State the blood parasite species.
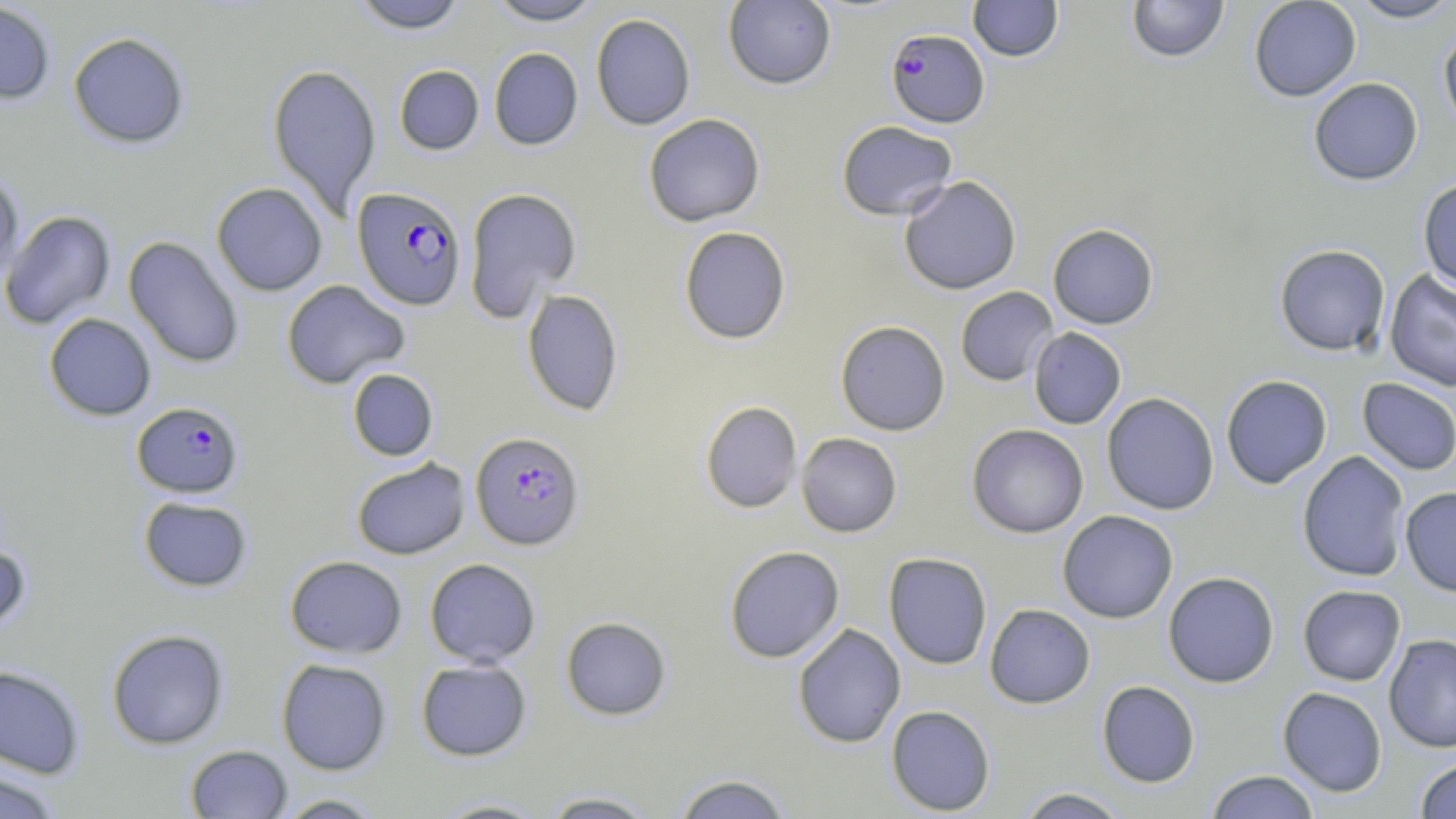
Plasmodium falciparum.

field of view = one of a larger specimen
magnification = 1000x
stain = May-Grünwald-Giemsa
uninfected red blood cell locations = approximate bounding boxes as [x1, y1, x2, y2] in pixels: [486, 0, 603, 25], [723, 0, 837, 90], [967, 0, 1064, 62], [1127, 0, 1229, 63], [1248, 0, 1362, 102], [1347, 0, 1456, 23], [0, 1, 57, 105], [350, 1, 468, 33], [590, 13, 696, 130], [1439, 27, 1456, 138], [68, 31, 190, 149], [489, 47, 583, 150], [267, 63, 382, 219], [394, 65, 484, 155], [1308, 77, 1423, 186], [643, 113, 765, 226], [836, 120, 958, 221], [0, 172, 25, 287], [898, 176, 1021, 295], [1418, 178, 1456, 293], [211, 182, 328, 296], [463, 187, 581, 322], [1, 210, 116, 330], [1047, 224, 1159, 329], [678, 226, 791, 344], [123, 235, 244, 369], [1274, 244, 1391, 357], [1385, 270, 1456, 391], [281, 279, 410, 389], [955, 286, 1058, 387], [522, 289, 624, 416], [43, 313, 156, 420], [835, 320, 950, 436], [1028, 327, 1126, 429], [347, 369, 438, 461], [1220, 374, 1332, 489], [1357, 378, 1456, 476], [1102, 392, 1219, 515], [700, 401, 803, 514], [966, 424, 1089, 538], [796, 433, 902, 537], [1297, 451, 1410, 582], [351, 457, 470, 560], [1400, 486, 1456, 597], [138, 496, 253, 592], [1057, 510, 1178, 623], [0, 541, 32, 638], [723, 545, 845, 663], [883, 552, 992, 669], [284, 555, 407, 658], [424, 558, 541, 667], [1163, 571, 1280, 688], [1298, 584, 1406, 686], [984, 603, 1095, 709], [560, 616, 671, 720], [792, 624, 906, 748], [106, 628, 229, 749], [1384, 633, 1456, 753], [276, 658, 392, 775], [415, 658, 532, 761], [0, 664, 86, 779], [1096, 680, 1200, 787], [1278, 687, 1387, 796], [886, 704, 996, 816], [185, 744, 292, 818], [1415, 757, 1456, 818], [0, 769, 62, 819], [1205, 770, 1320, 818], [671, 773, 794, 818], [1013, 787, 1131, 818], [539, 791, 660, 818], [272, 794, 386, 818], [428, 797, 553, 818]
Plasmodium falciparum-infected red blood cell locations = approximate bounding boxes as [x1, y1, x2, y2] in pixels: [886, 28, 989, 127], [352, 186, 467, 310], [132, 401, 244, 498], [470, 431, 584, 550]
image size = 1456×819 pixels
preparation = thin blood smear
modality = light microscopy